Locate every blood parasite and identify its species.
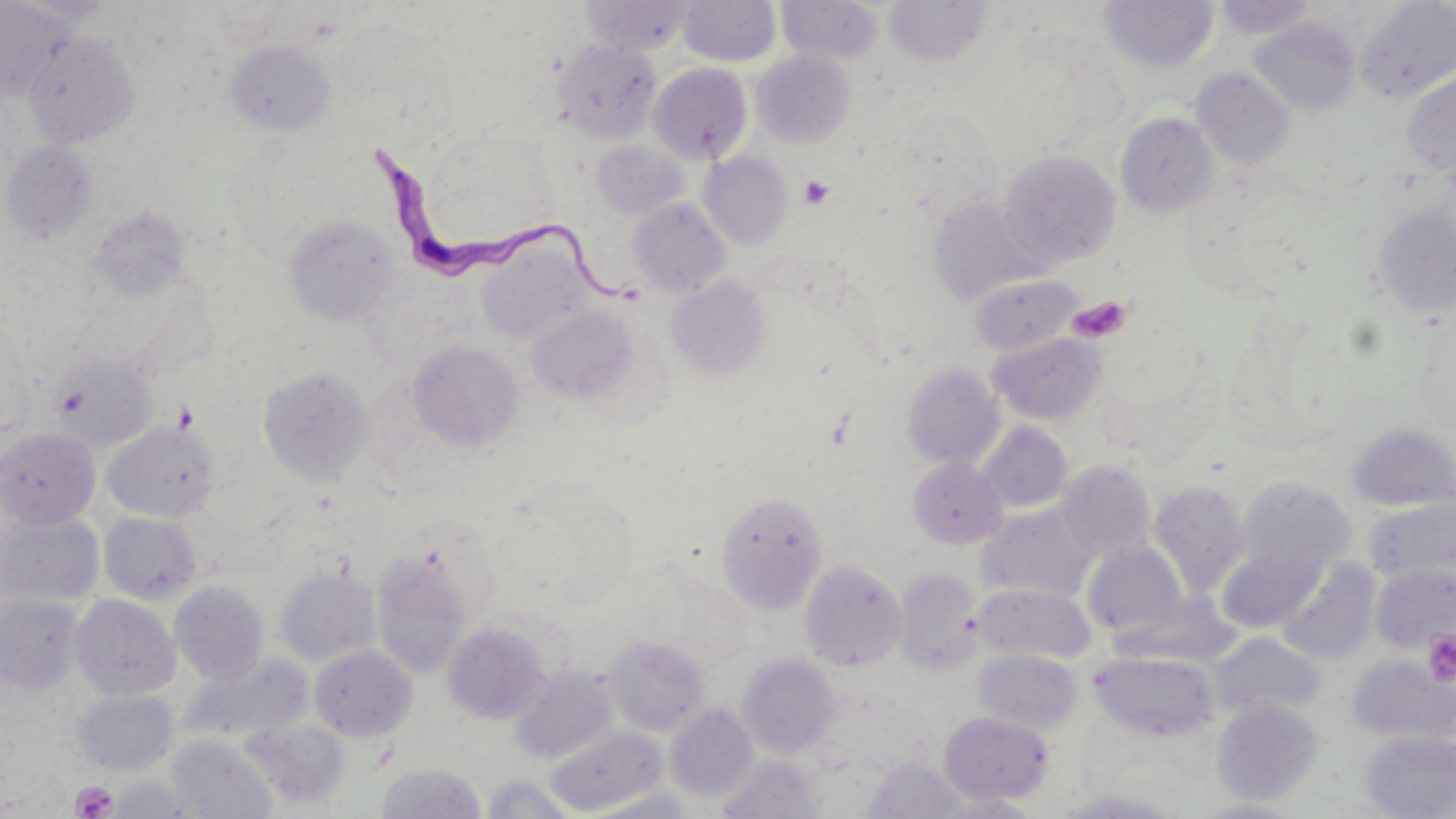

Approximate bounding boxes as (x1, y1, x2, y2) in pixels.
Trypanosoma brucei: (365, 133, 641, 314).
No Plasmodium falciparum, Plasmodium ovale, Plasmodium malariae, Plasmodium vivax, or Babesia divergens observed.

Uninfected red blood cell locations: (15, 0, 118, 24), (580, 0, 696, 55), (1099, 0, 1219, 72), (1211, 0, 1320, 40), (0, 1, 73, 100), (678, 1, 781, 66), (777, 1, 884, 64), (884, 1, 994, 66), (1354, 2, 1456, 102), (1249, 18, 1361, 117), (23, 32, 140, 149), (551, 39, 661, 145), (225, 41, 335, 136), (751, 50, 855, 148), (648, 63, 753, 164), (1191, 67, 1296, 170), (1401, 68, 1456, 181), (897, 107, 1004, 222), (1115, 112, 1220, 218), (591, 140, 691, 220), (2, 141, 98, 243), (999, 150, 1121, 268), (698, 151, 794, 250), (628, 198, 732, 297), (927, 198, 1045, 305), (1373, 205, 1456, 316), (87, 207, 192, 302), (283, 214, 399, 325), (476, 238, 595, 346), (969, 274, 1081, 355), (666, 276, 772, 380), (526, 305, 636, 404), (988, 332, 1107, 426), (408, 340, 525, 453), (49, 352, 158, 452), (901, 364, 1004, 469), (257, 365, 375, 485), (102, 419, 220, 523), (1347, 421, 1456, 512), (977, 422, 1073, 513), (0, 427, 100, 529), (908, 457, 1008, 549), (1055, 460, 1156, 563), (1235, 476, 1356, 580), (1149, 481, 1248, 597), (716, 492, 828, 613), (1365, 497, 1456, 588), (975, 504, 1095, 603), (0, 511, 105, 607), (99, 511, 203, 604), (1083, 542, 1189, 638), (1218, 544, 1324, 633), (371, 552, 473, 679), (1275, 558, 1381, 664), (800, 560, 907, 671), (1370, 565, 1456, 655), (275, 568, 381, 666), (894, 568, 985, 675), (169, 581, 270, 686), (972, 583, 1095, 664), (0, 593, 84, 695), (1118, 593, 1238, 667), (70, 594, 181, 700), (441, 622, 550, 724), (1212, 633, 1325, 720), (604, 635, 712, 736), (309, 646, 417, 741), (974, 649, 1083, 735), (1088, 651, 1220, 741), (181, 655, 314, 747), (738, 655, 841, 758), (1348, 655, 1455, 744), (510, 666, 619, 764), (71, 689, 179, 776), (1212, 698, 1324, 805), (665, 703, 759, 801), (939, 711, 1054, 806), (239, 718, 350, 809), (546, 724, 668, 816), (1360, 731, 1456, 818), (168, 736, 277, 819), (717, 755, 826, 818), (860, 758, 971, 818), (376, 762, 487, 818), (480, 774, 580, 818), (106, 775, 199, 818), (585, 788, 701, 818), (933, 793, 1046, 818), (1196, 799, 1307, 818). Platelet locations: (799, 175, 836, 210), (1066, 296, 1133, 344), (173, 399, 200, 435), (1422, 630, 1456, 686), (70, 780, 118, 819). Slide-level diagnosis: Trypanosoma brucei. One field of a larger specimen. Captured at 1000x magnification. Optical microscopy. Thin blood smear. May-Grünwald-Giemsa stain. Image is 1456×819 pixels.